Outline each P. falciparum parasite and classify it by life-cycle stage.
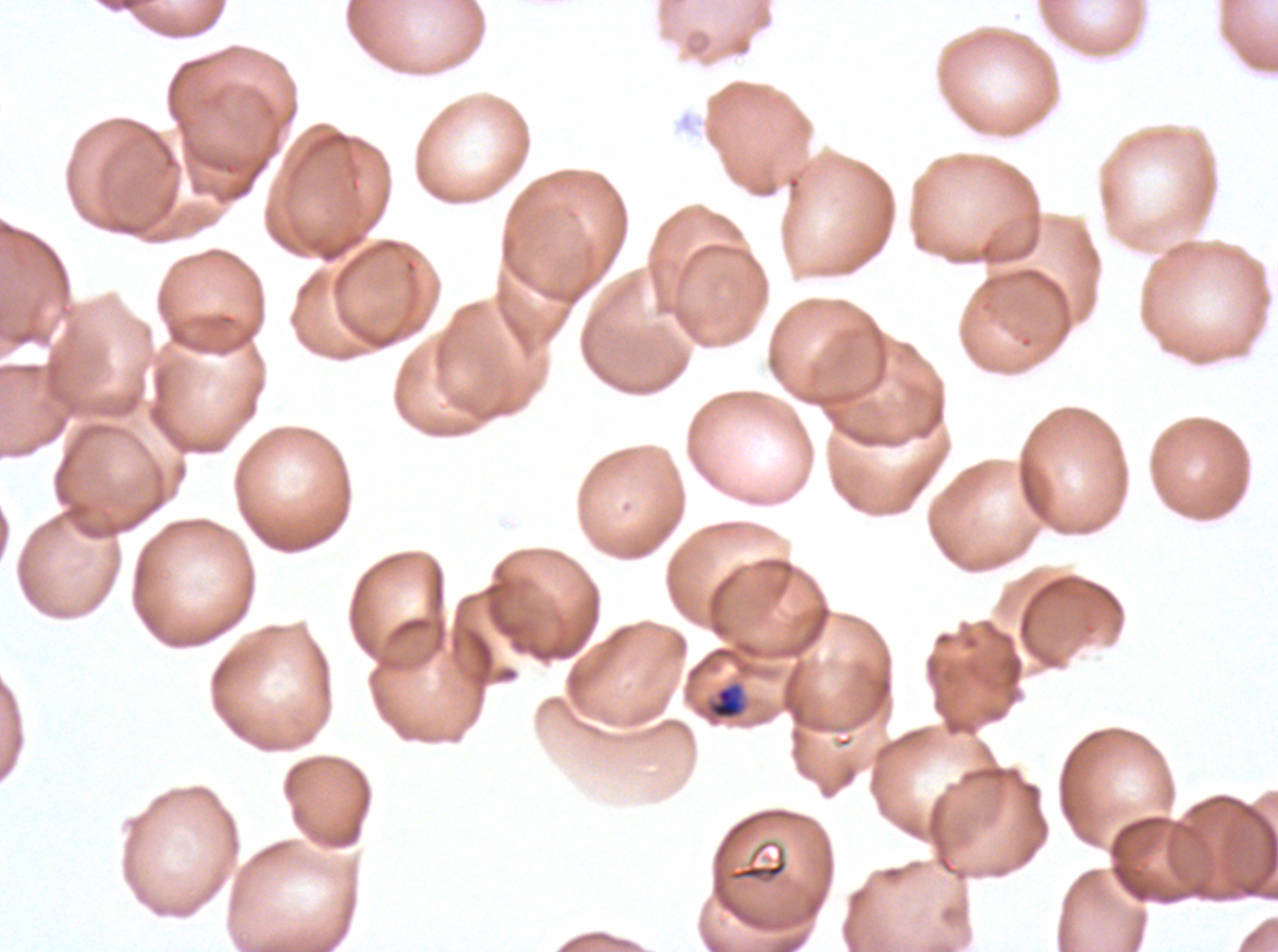

Approximate bounding rectangles given as corner coordinates in pixels from the top-left.
Mid trophozoites: (x1=707, y1=683, x2=745, y2=720).
No rings, late-ring/early-trophozoite forms, late trophozoites, early schizonts, late schizonts, segmenters, or gametocytes observed.

Summary:
  - Stain: Giemsa
  - Specimen: ex-vivo P. falciparum culture from a patient in The Gambia, grown for 24 to 48 hours
  - Image size: 1278×952 pixels
  - Field of view: sub-image separated from a larger composite
  - Preparation: thin blood smear